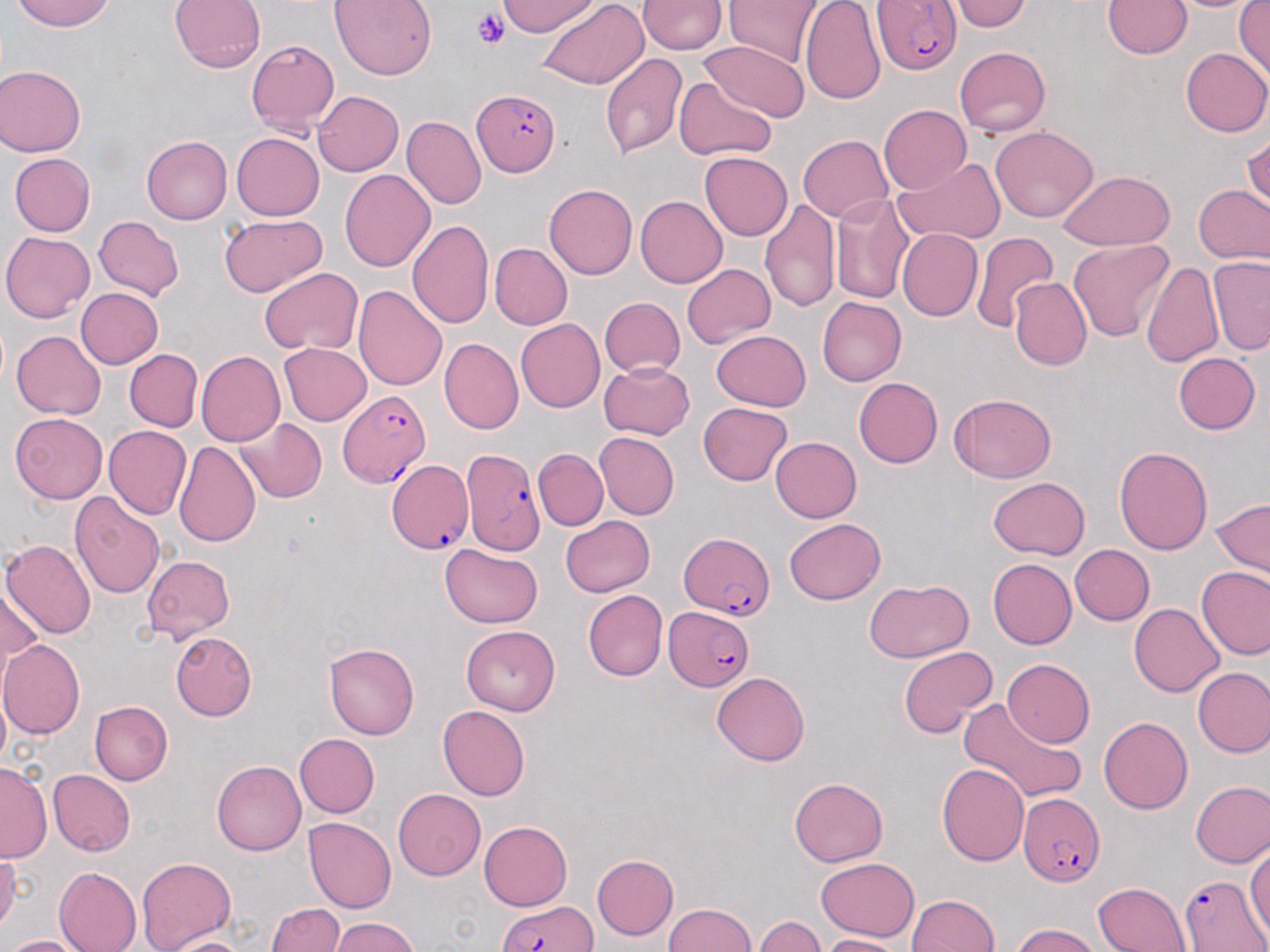

Summary:
  - Coordinate format: approximate bounding boxes as (x1, y1, x2, y2) in pixels
  - Plasmodium falciparum-infected red blood cell locations: (873, 0, 963, 74), (472, 89, 562, 176), (336, 389, 431, 489), (462, 449, 546, 557), (387, 460, 473, 554), (678, 532, 772, 619), (662, 606, 755, 693), (1017, 793, 1105, 886), (1177, 874, 1269, 949), (495, 903, 597, 952)
  - Platelet locations: (474, 8, 509, 50)
  - Uninfected red blood cell locations: (11, 0, 117, 32), (167, 0, 267, 76), (330, 0, 437, 79), (499, 0, 599, 38), (799, 0, 886, 105), (950, 0, 1031, 31), (1172, 0, 1258, 14), (641, 1, 726, 55), (727, 1, 819, 65), (1103, 1, 1189, 58), (539, 2, 647, 90), (1233, 2, 1270, 82), (246, 40, 339, 136), (701, 42, 806, 122), (1182, 47, 1270, 138), (954, 48, 1052, 136), (599, 51, 688, 162), (0, 64, 82, 157), (676, 74, 775, 160), (312, 89, 403, 176), (879, 105, 970, 196), (401, 116, 486, 208), (991, 128, 1097, 222), (231, 131, 325, 219), (799, 134, 895, 223), (1242, 134, 1270, 208), (141, 137, 232, 224), (701, 150, 793, 241), (10, 154, 96, 235), (893, 157, 1005, 245), (340, 169, 435, 272), (1056, 170, 1176, 250), (545, 184, 637, 277), (1192, 184, 1270, 264), (829, 193, 917, 304), (637, 194, 729, 287), (761, 199, 840, 316), (218, 213, 330, 296), (93, 216, 185, 299), (408, 217, 494, 332), (898, 229, 981, 322), (0, 230, 92, 322), (970, 233, 1057, 335), (1068, 237, 1174, 342), (489, 243, 572, 330), (1207, 256, 1270, 355), (1142, 260, 1224, 371), (681, 262, 774, 347), (257, 266, 362, 355), (1011, 279, 1089, 370), (352, 283, 449, 392), (74, 287, 163, 370), (598, 297, 685, 377), (816, 297, 906, 386), (515, 318, 606, 412), (11, 330, 106, 418), (710, 330, 812, 410), (441, 338, 522, 433), (280, 342, 372, 426), (125, 348, 202, 430), (197, 351, 286, 445), (1173, 352, 1257, 433), (600, 359, 695, 439), (852, 376, 943, 468), (948, 393, 1057, 483), (698, 402, 794, 487), (10, 413, 107, 503), (233, 416, 327, 502), (105, 425, 192, 521), (592, 432, 679, 519), (771, 436, 863, 522), (173, 440, 259, 548), (1115, 445, 1212, 558), (535, 447, 607, 530), (987, 477, 1088, 559), (70, 490, 165, 598), (1208, 497, 1269, 575), (562, 514, 655, 595), (785, 517, 885, 604), (0, 537, 95, 639), (438, 544, 544, 627), (1070, 544, 1154, 624), (140, 554, 235, 641), (988, 558, 1077, 649), (1197, 566, 1270, 662), (863, 578, 974, 663), (583, 589, 667, 681), (0, 590, 38, 688), (1129, 603, 1224, 695), (462, 623, 563, 714), (169, 632, 258, 721), (0, 640, 83, 740), (324, 642, 419, 740), (897, 645, 996, 740), (1002, 657, 1093, 748), (1193, 666, 1270, 757), (712, 670, 812, 764), (90, 700, 172, 784), (956, 700, 1086, 805), (439, 705, 530, 801), (1098, 716, 1194, 813), (296, 733, 380, 818), (212, 760, 305, 855), (0, 762, 49, 860), (937, 762, 1031, 865), (50, 769, 136, 856), (789, 777, 890, 867), (1190, 780, 1269, 869), (392, 790, 485, 880), (305, 817, 399, 912), (480, 820, 576, 910), (1246, 843, 1270, 943), (0, 852, 23, 934), (590, 853, 678, 941), (135, 857, 238, 952), (814, 859, 917, 942), (54, 867, 140, 951), (1092, 881, 1193, 952), (909, 893, 998, 952), (268, 903, 348, 952), (660, 904, 759, 952), (754, 914, 826, 952), (328, 918, 422, 952), (1009, 926, 1104, 952), (168, 931, 248, 952), (4, 934, 87, 952), (818, 934, 898, 951)
  - Slide-level diagnosis: Plasmodium falciparum
  - Image size: 1270×952 pixels
  - Magnification: 1000x
  - Modality: optical microscopy
  - Field of view: one of a larger specimen
  - Stain: May-Grünwald-Giemsa
  - Preparation: thin blood film